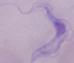 Photomicrograph. 1000x magnification. A trypanosome is seen.